Classify this cell by malaria status.
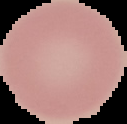
It is uninfected.

Summary:
  - Image type: cell region segmented out of the field of view; surrounding area masked to black
  - Preparation: thin blood smear
  - Image size: 127×124 pixels